Name the cell type shown.
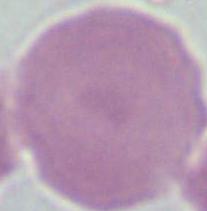
This is an erythrocyte.

modality = photomicrograph
magnification = 1000x